Describe the morphology of the red blood cells.
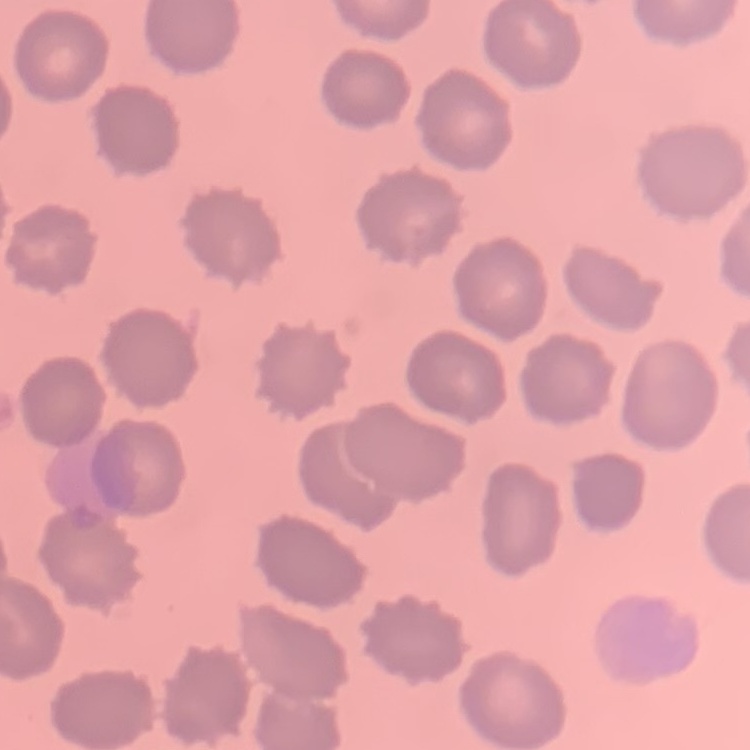
No rouleaux formation.

{
  "preparation": "thin peripheral smear",
  "image_type": "square crop of a larger photomicrograph",
  "stain": "Field's or Giemsa"
}